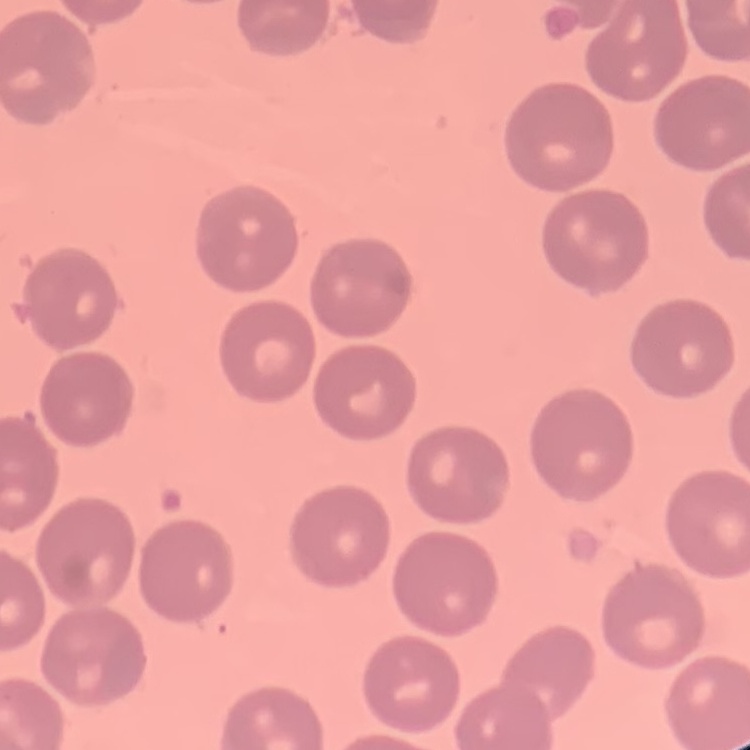
The red blood cells exhibit no rouleaux formation. One tile cut from a larger photomicrograph. Thin peripheral smear. Field's or Giemsa stain.